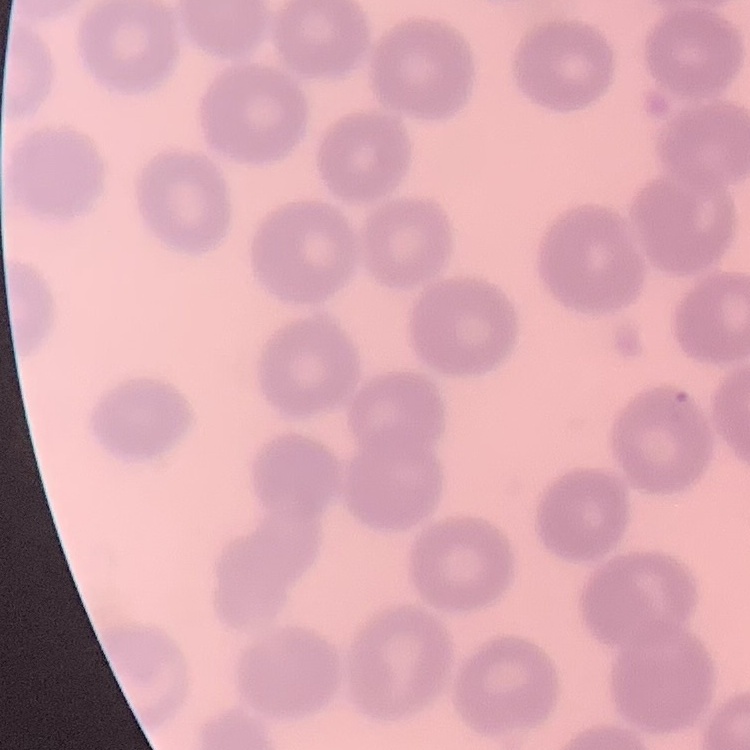

erythrocyte morphology = no rouleaux formation
stain = Field's or Giemsa
preparation = thin blood smear
image type = square crop of a larger photomicrograph